Report the malaria status of this cell.
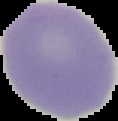

Uninfected.

preparation: thin blood film
image_type: cell region segmented out of the field of view; surrounding area masked to black
image_size: 118×121 pixels